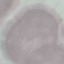

malaria status = uninfected
image type = automatically extracted cell patch, resized to 64 × 64 pixels
capture = smartphone through the microscope eyepiece
stain = Giemsa
preparation = thin smear